Locate every leukocyte (white blood cell).
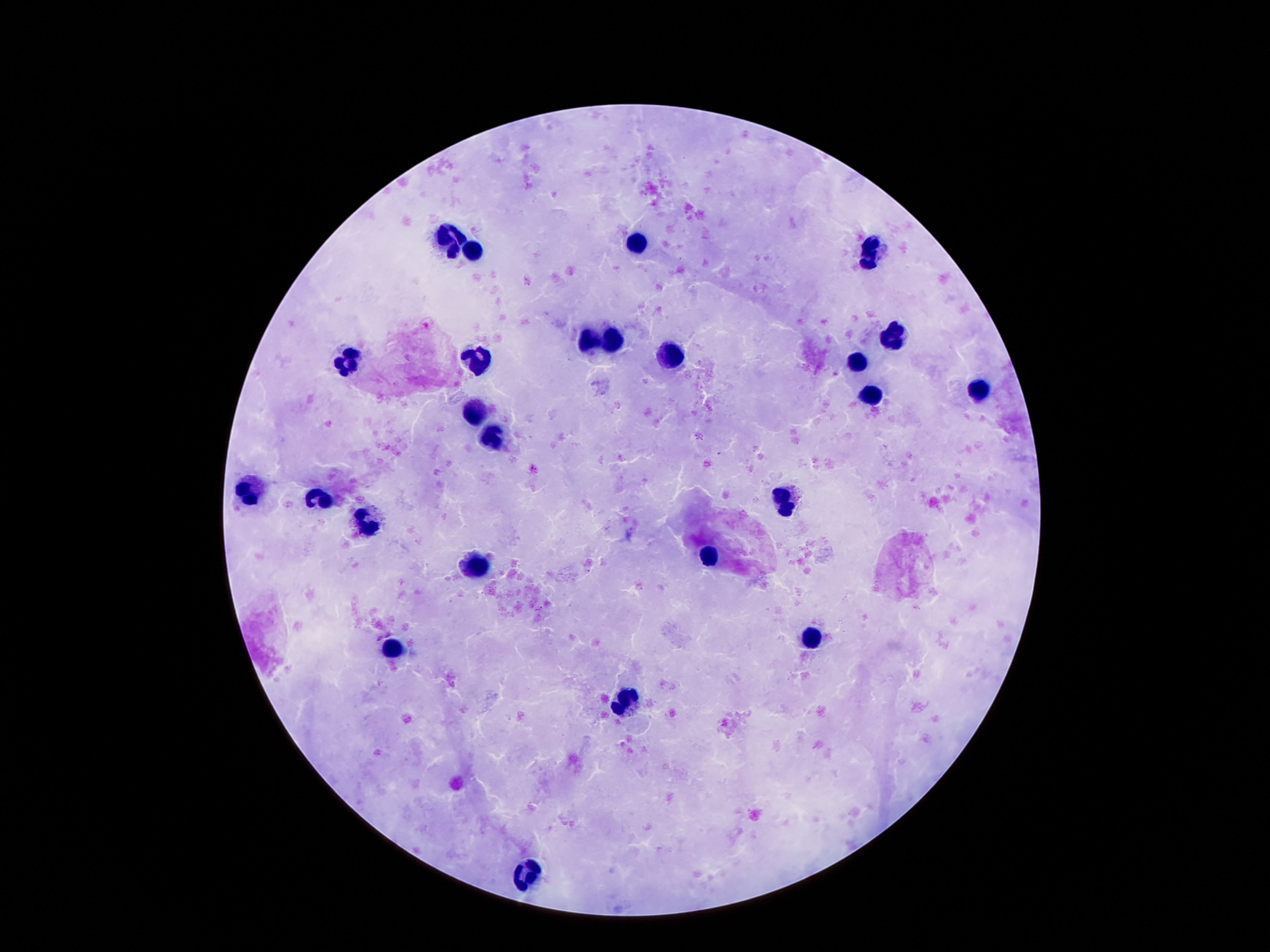
Approximate object centers, in pixels from the top-left corner.
Leukocytes: (x=451, y=238), (x=637, y=241), (x=871, y=247), (x=473, y=251), (x=895, y=335), (x=616, y=338), (x=587, y=341), (x=676, y=351), (x=474, y=360), (x=349, y=362), (x=857, y=362), (x=977, y=391), (x=873, y=394), (x=474, y=412), (x=494, y=438), (x=247, y=488), (x=787, y=499), (x=322, y=501), (x=369, y=524), (x=709, y=556), (x=474, y=569), (x=812, y=636), (x=394, y=649), (x=623, y=706), (x=528, y=870).

preparation = thick peripheral-blood smear
magnification = 100x
field of view = one from this slide
image size = 1270×952 pixels
capture = smartphone camera through the microscope eyepiece
stain = Giemsa
patient malaria status = not infected